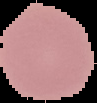

Cell region segmented out of the field of view; the surrounding area is masked to black. From a thin blood film. Image is 97×103 pixels. Result: no malaria parasites seen.